Name the cell type shown.
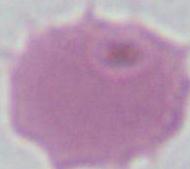

An erythrocyte.

Summary:
  - Magnification: 1000x
  - Modality: micrograph